Assess the morphology of the erythrocytes.
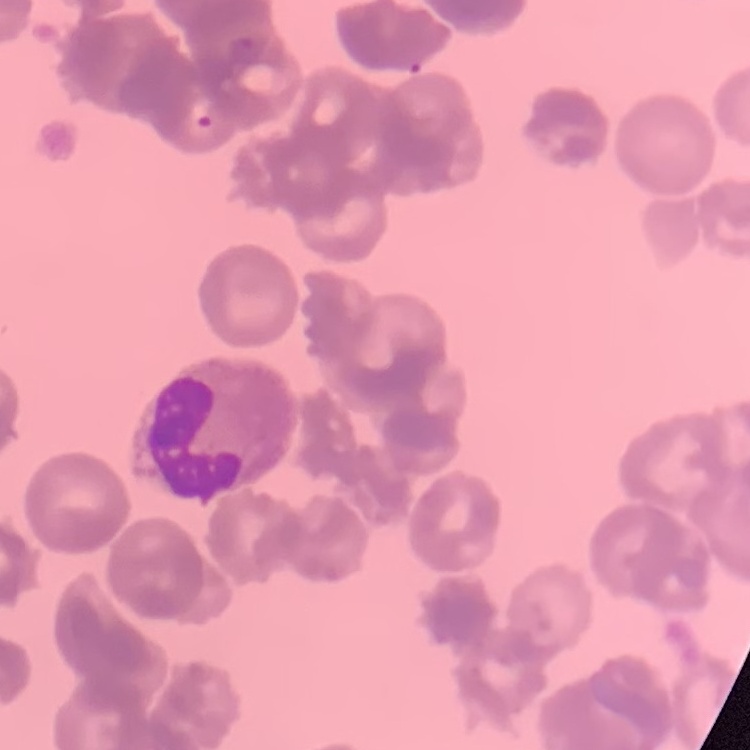
Rouleaux formation.

Summary:
  - Image type: one tile cut from a larger photomicrograph
  - Preparation: thin peripheral smear
  - Stain: Field's or Giemsa